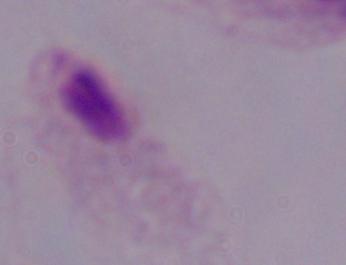
Summary:
  - Magnification: 1000x
  - Identification: trichomonad
  - Modality: micrograph